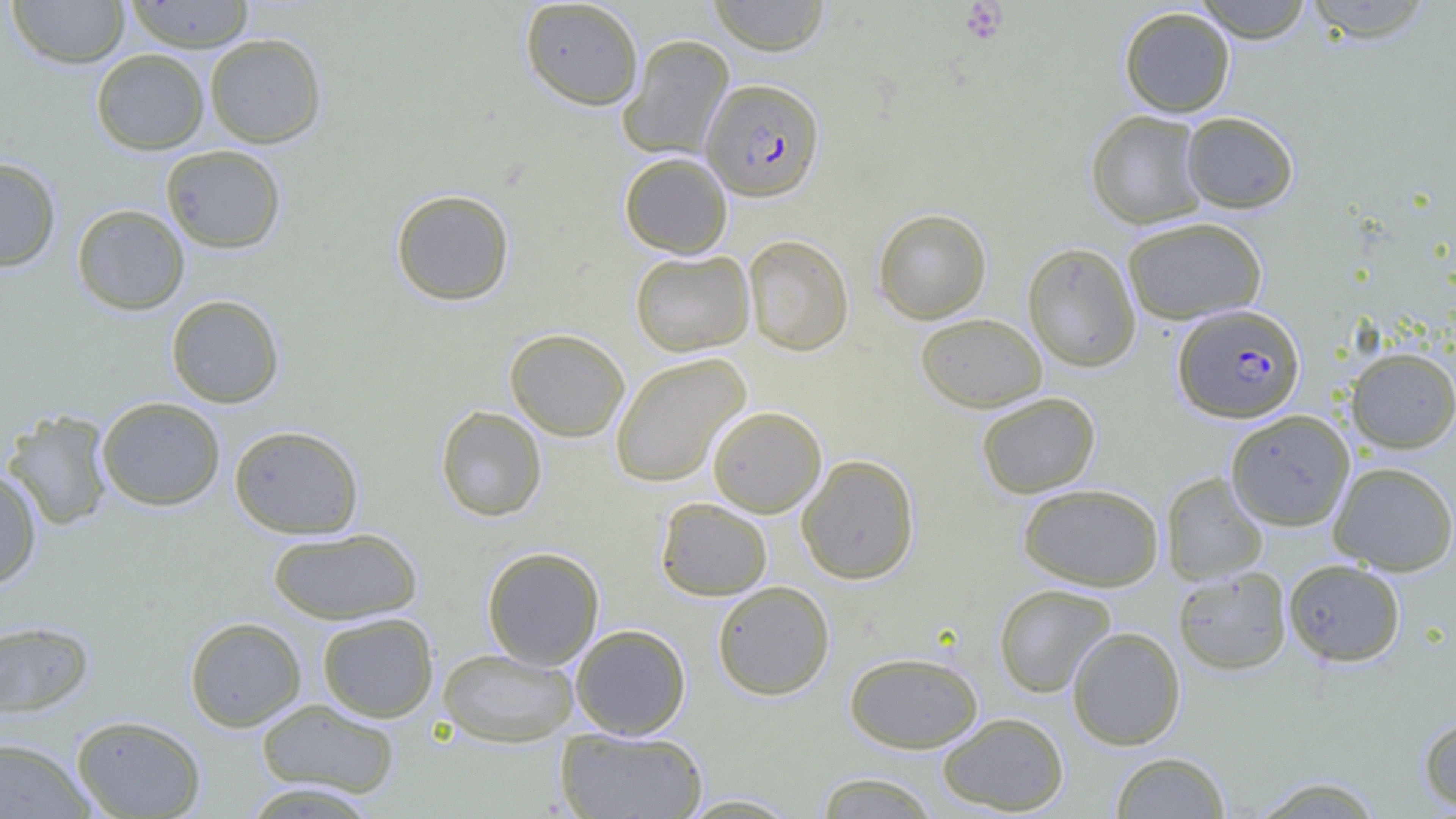

Approximate bounding boxes as (x1, y1, x2, y2) in pixels. Uninfected red blood cell locations: (7, 0, 130, 69), (123, 0, 255, 53), (520, 0, 644, 111), (707, 0, 830, 56), (1192, 0, 1315, 43), (1302, 0, 1436, 43), (1118, 6, 1236, 117), (204, 32, 327, 148), (618, 34, 734, 161), (91, 49, 210, 155), (1085, 110, 1208, 230), (1180, 111, 1299, 213), (160, 145, 287, 254), (619, 152, 732, 258), (0, 158, 62, 272), (390, 188, 515, 306), (71, 204, 190, 315), (872, 208, 992, 324), (1122, 217, 1268, 324), (742, 234, 854, 355), (1022, 242, 1141, 372), (630, 250, 755, 356), (166, 294, 285, 408), (915, 312, 1047, 412), (504, 327, 630, 441), (1345, 347, 1456, 453), (609, 352, 751, 488), (975, 392, 1100, 498), (96, 396, 226, 511), (435, 405, 547, 522), (707, 405, 827, 517), (2, 409, 115, 530), (1225, 409, 1355, 531), (228, 424, 364, 539), (796, 454, 920, 585), (1328, 461, 1456, 575), (0, 466, 42, 590), (1160, 471, 1269, 586), (1017, 482, 1164, 592), (655, 497, 773, 601), (266, 527, 423, 625), (481, 546, 604, 670), (1283, 559, 1406, 667), (1172, 566, 1292, 675), (712, 580, 835, 700), (993, 583, 1117, 698), (316, 612, 439, 722), (184, 616, 307, 732), (0, 619, 95, 718), (570, 624, 691, 739), (1066, 626, 1186, 750), (437, 647, 579, 747), (844, 651, 984, 753), (255, 698, 401, 799), (937, 711, 1070, 815), (71, 714, 207, 818), (1418, 714, 1456, 812), (555, 727, 708, 818), (0, 737, 95, 818), (1110, 751, 1231, 818), (812, 771, 942, 818), (1249, 774, 1386, 818), (237, 781, 384, 818), (676, 793, 805, 817). Plasmodium falciparum-infected red blood cell locations: (701, 78, 825, 202), (1173, 304, 1305, 423). Platelet locations: (959, 1, 1008, 44). Slide-level diagnosis: Plasmodium falciparum. Single field of view. 1000x magnification. Thin blood smear. Image is 1456×819 pixels. Light microscopy.